Assess this cell for malaria.
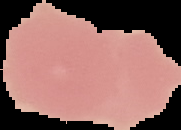

Uninfected.

Summary:
  - Image type: cell region segmented out of the field of view; surrounding area masked to black
  - Image size: 181×130 pixels
  - Preparation: thin blood smear